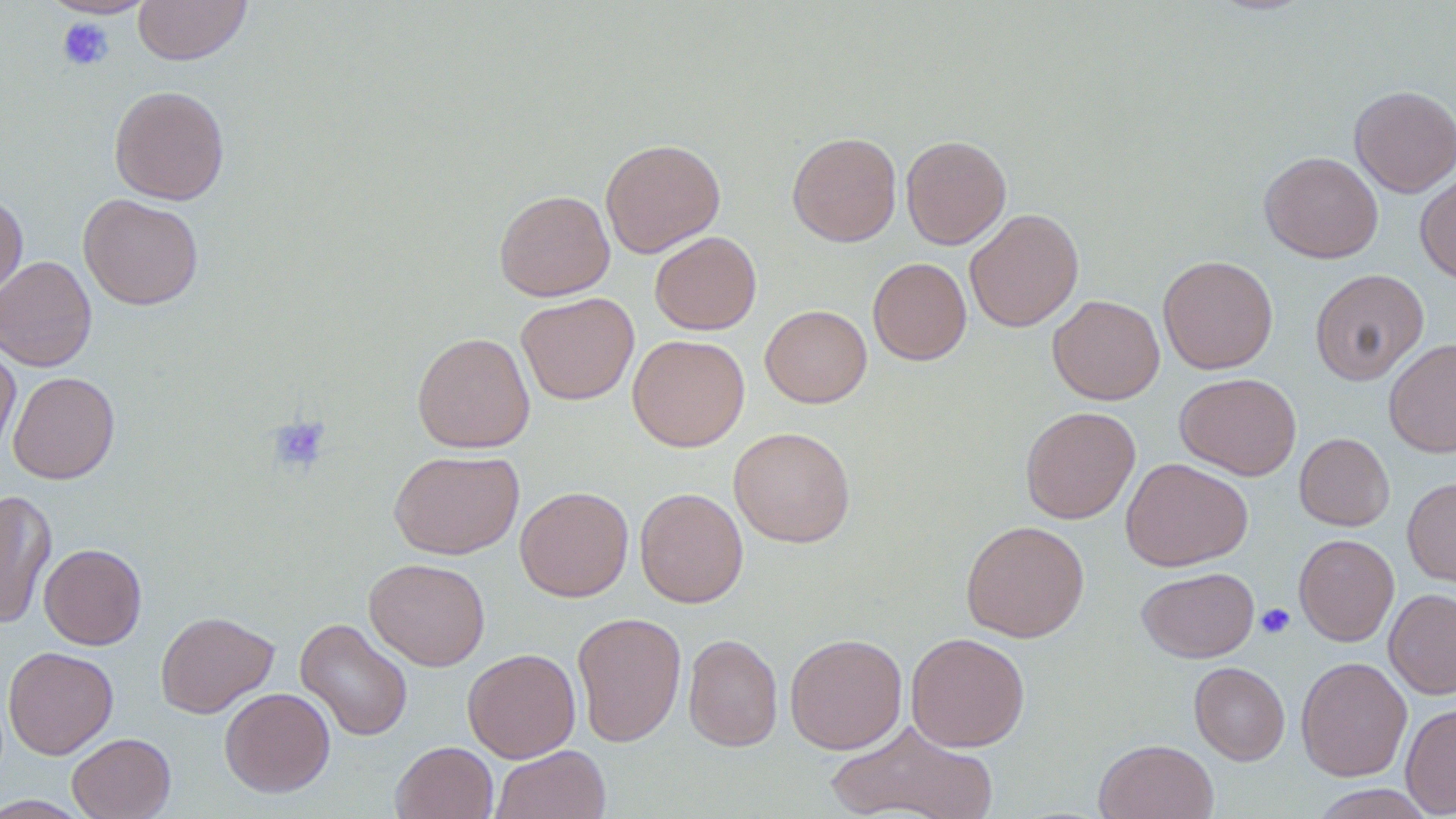 Approximate bounding boxes as (x1,y1)-(x2,y2) corner pairs in pixels. Uninfected red blood cell locations: (42,0)-(158,18), (133,0)-(252,65), (109,85)-(230,205), (1349,85)-(1456,197), (787,132)-(902,247), (900,134)-(1011,249), (600,138)-(726,258), (1260,151)-(1383,263), (1415,169)-(1456,284), (494,189)-(615,301), (0,193)-(28,302), (79,193)-(204,310), (964,208)-(1084,332), (650,231)-(761,335), (1157,254)-(1278,374), (0,255)-(97,372), (868,257)-(971,365), (1309,268)-(1429,385), (516,292)-(639,405), (1047,294)-(1165,405), (760,304)-(872,408), (411,332)-(535,453), (627,334)-(749,452), (1384,337)-(1456,458), (0,340)-(20,461), (8,371)-(120,484), (1175,373)-(1301,480), (1020,406)-(1140,524), (729,426)-(856,548), (1294,433)-(1395,531), (389,450)-(524,560), (1120,457)-(1253,572), (1402,476)-(1456,587), (515,486)-(633,602), (634,487)-(749,607), (0,488)-(57,630), (961,519)-(1089,642), (1294,534)-(1399,646), (39,543)-(147,650), (364,557)-(490,671), (1137,567)-(1259,662), (1384,588)-(1456,700), (156,610)-(279,717), (572,612)-(686,747), (295,618)-(413,741), (785,632)-(907,754), (905,632)-(1031,752), (683,633)-(783,752), (3,646)-(118,759), (462,648)-(581,763), (1295,656)-(1412,781), (1189,662)-(1290,765), (220,687)-(335,797), (1400,702)-(1456,817), (825,720)-(999,819), (67,732)-(176,819), (1094,739)-(1218,819), (391,741)-(498,819), (490,745)-(611,819), (1308,784)-(1436,818), (0,796)-(93,818). Platelet locations: (56,18)-(114,71), (268,416)-(331,474), (1256,603)-(1295,639). Slide-level diagnosis: no evidence of blood parasites. Thin blood smear. Light microscopy. Image is 1456×819 pixels. May-Grünwald-Giemsa stain. One field of a larger specimen. Captured at 1000x magnification.